Locate every Plasmodium falciparum-infected red blood cell.
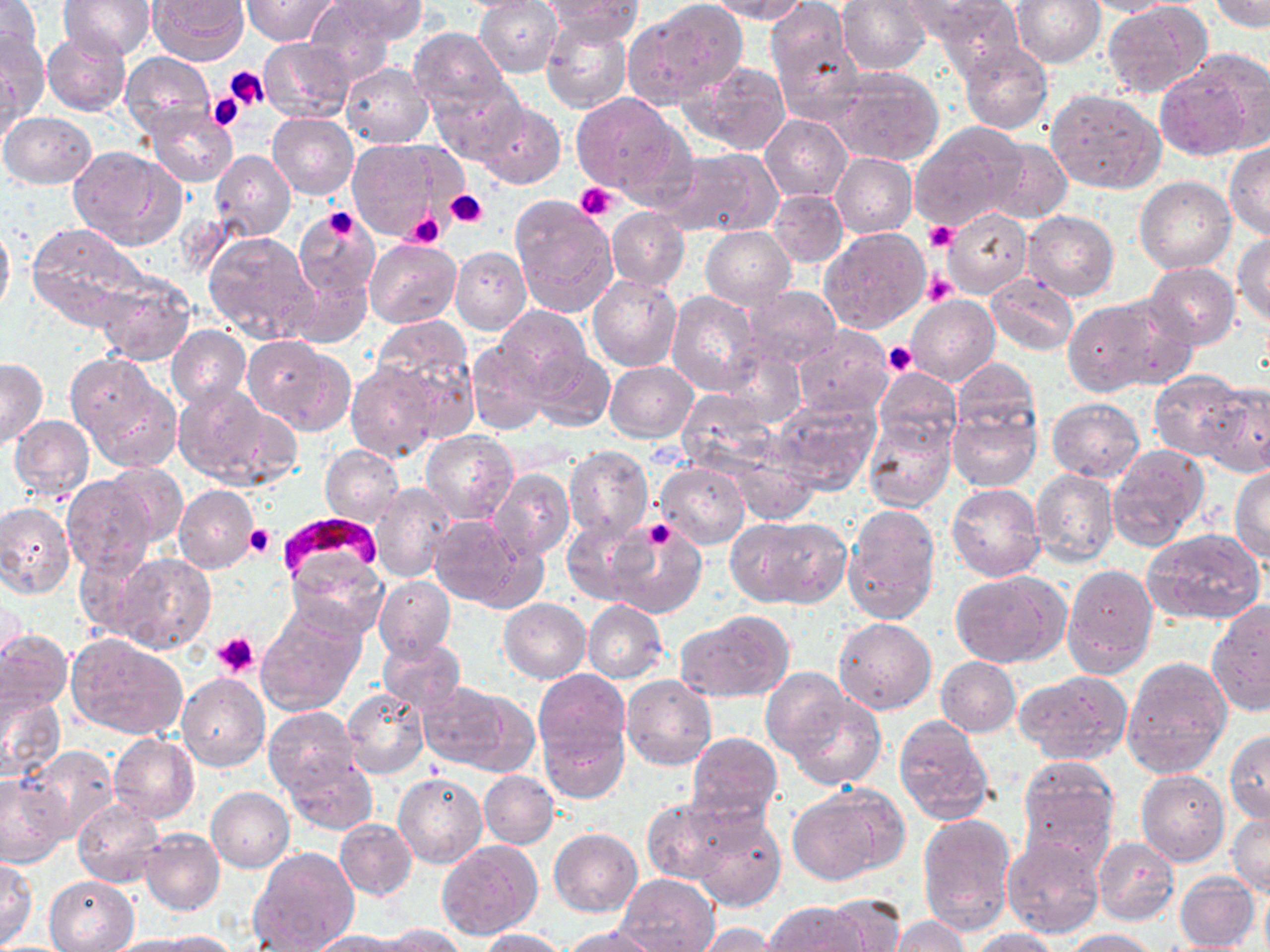

Approximate bounding boxes as [x1, y1, x2, y2] in pixels.
Plasmodium falciparum-infected red blood cells: [283, 513, 380, 578].

slide-level diagnosis = Plasmodium falciparum
stain = May-Grünwald-Giemsa
magnification = 1000x
preparation = thin blood smear
field of view = single
platelet locations = approximate bounding boxes as [x1, y1, x2, y2] in pixels: [225, 67, 270, 111], [209, 93, 246, 131], [575, 182, 619, 221], [445, 190, 488, 229], [321, 206, 359, 239], [406, 212, 444, 247], [925, 222, 956, 252], [923, 271, 957, 307], [883, 342, 916, 377], [642, 519, 675, 551], [245, 523, 275, 558], [213, 631, 261, 677]
uninfected red blood cell locations = approximate bounding boxes as [x1, y1, x2, y2] in pixels: [0, 0, 42, 70], [148, 0, 247, 65], [244, 0, 337, 45], [304, 0, 398, 86], [335, 0, 427, 43], [446, 0, 551, 13], [475, 0, 563, 76], [542, 0, 644, 44], [708, 0, 808, 23], [765, 0, 860, 120], [836, 0, 931, 75], [1010, 0, 1106, 68], [1078, 0, 1180, 16], [59, 1, 155, 60], [630, 1, 746, 104], [901, 1, 1009, 45], [1101, 1, 1210, 101], [1208, 1, 1270, 30], [931, 5, 1025, 81], [541, 17, 633, 113], [408, 27, 510, 118], [0, 29, 48, 133], [42, 32, 131, 116], [260, 38, 356, 123], [957, 42, 1054, 135], [120, 53, 214, 139], [1, 54, 24, 150], [1155, 57, 1265, 160], [684, 60, 792, 155], [340, 63, 433, 148], [824, 65, 946, 167], [431, 80, 524, 164], [1046, 87, 1165, 193], [570, 93, 679, 196], [473, 101, 565, 189], [144, 107, 238, 187], [1, 112, 97, 189], [268, 113, 358, 199], [760, 114, 852, 201], [911, 122, 1026, 230], [348, 138, 450, 239], [984, 138, 1072, 223], [1224, 143, 1270, 239], [69, 146, 187, 251], [662, 147, 782, 237], [210, 149, 294, 241], [830, 153, 917, 238], [1134, 176, 1236, 274], [768, 190, 847, 267], [509, 194, 618, 320], [292, 205, 379, 301], [607, 207, 690, 291], [943, 208, 1032, 298], [1023, 211, 1119, 301], [0, 219, 13, 319], [26, 223, 148, 329], [701, 227, 795, 307], [819, 227, 931, 333], [203, 231, 320, 346], [1233, 232, 1270, 325], [363, 238, 461, 327], [451, 246, 531, 334], [1144, 262, 1240, 349], [289, 264, 370, 349], [94, 272, 196, 365], [1102, 273, 1231, 373], [588, 274, 682, 371], [986, 274, 1079, 355], [738, 286, 844, 370], [668, 291, 764, 396], [907, 295, 1000, 387], [1062, 301, 1165, 395], [493, 306, 591, 393], [371, 315, 477, 426], [167, 324, 250, 409], [793, 325, 895, 419], [242, 337, 352, 432], [464, 338, 551, 436], [721, 346, 805, 426], [529, 347, 614, 431], [68, 356, 178, 468], [951, 357, 1040, 445], [0, 358, 46, 447], [346, 361, 439, 462], [605, 362, 698, 442], [873, 367, 962, 454], [1148, 372, 1247, 461], [174, 382, 289, 487], [1201, 383, 1270, 478], [773, 395, 880, 495], [1047, 397, 1145, 482], [949, 409, 1040, 491], [862, 414, 956, 511], [10, 415, 94, 499], [421, 431, 520, 526], [1106, 443, 1208, 552], [725, 444, 819, 522], [319, 445, 404, 526], [564, 446, 652, 544], [656, 462, 749, 547], [104, 463, 187, 548], [1230, 466, 1270, 561], [1031, 469, 1119, 565], [488, 470, 575, 560], [62, 475, 157, 576], [370, 482, 459, 584], [947, 483, 1044, 582], [174, 485, 259, 573], [0, 501, 75, 598], [843, 504, 940, 624], [428, 514, 537, 609], [727, 515, 851, 609], [562, 519, 650, 605], [608, 521, 706, 618], [1143, 528, 1267, 625], [285, 547, 386, 638], [74, 548, 157, 638], [112, 553, 215, 653], [1062, 564, 1158, 679], [949, 571, 1068, 669], [374, 576, 455, 660], [498, 598, 591, 682], [1206, 599, 1269, 715], [583, 600, 666, 682], [256, 609, 363, 716], [676, 609, 795, 703], [833, 617, 936, 714], [0, 628, 71, 715], [67, 633, 187, 739], [378, 636, 466, 715], [936, 656, 1021, 736], [1122, 656, 1233, 778], [760, 666, 849, 759], [532, 668, 630, 767], [1014, 670, 1133, 767], [178, 674, 270, 771], [621, 674, 717, 771], [417, 683, 512, 769], [453, 687, 541, 776], [342, 688, 430, 779], [0, 689, 68, 784], [784, 690, 885, 790], [263, 706, 360, 794], [539, 717, 628, 803], [893, 717, 995, 824], [1225, 731, 1270, 825], [687, 732, 783, 828], [110, 734, 200, 822], [24, 746, 118, 842], [283, 755, 377, 834], [1019, 756, 1118, 860], [479, 770, 558, 848], [1137, 770, 1229, 865], [393, 773, 487, 869], [0, 774, 68, 864], [791, 784, 901, 881], [206, 786, 294, 872], [644, 798, 736, 885], [73, 801, 166, 888], [691, 811, 786, 912], [1228, 811, 1269, 898], [917, 814, 1017, 933], [336, 820, 417, 899], [549, 827, 642, 916], [140, 828, 225, 915], [1002, 835, 1104, 937], [1093, 836, 1179, 926], [438, 840, 542, 939], [252, 847, 359, 952], [1, 860, 38, 946], [1175, 870, 1260, 950], [617, 873, 719, 952], [44, 875, 139, 951], [1259, 882, 1270, 952], [823, 899, 905, 951], [764, 901, 869, 951], [890, 915, 969, 952], [690, 924, 777, 951], [380, 925, 468, 951], [563, 925, 660, 952], [478, 927, 566, 951], [970, 928, 1062, 952], [1065, 928, 1161, 951], [153, 931, 238, 951], [311, 931, 407, 952], [108, 934, 216, 952]
modality = light microscopy
image size = 1270×952 pixels